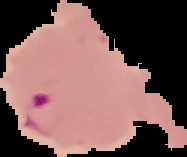

From a thin blood film. Malaria status: parasitized. Image is 187×157 pixels. Cell region segmented out of the field of view; the surrounding area is masked to black.